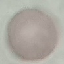
malaria status = uninfected
capture = smartphone through the microscope eyepiece
stain = Giemsa
image type = cell patch, automatically extracted from a larger field of view and resized to 64 × 64 pixels
preparation = thin smear